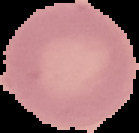

image size = 139×133 pixels
preparation = thin blood smear
image type = segmented cell region with the area outside set to black
result = negative for malaria parasites